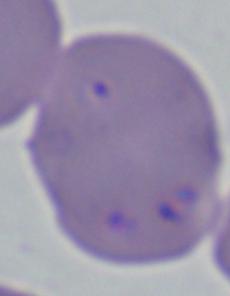

Micrograph. Captured at 1000x magnification. A Babesia parasite is seen.